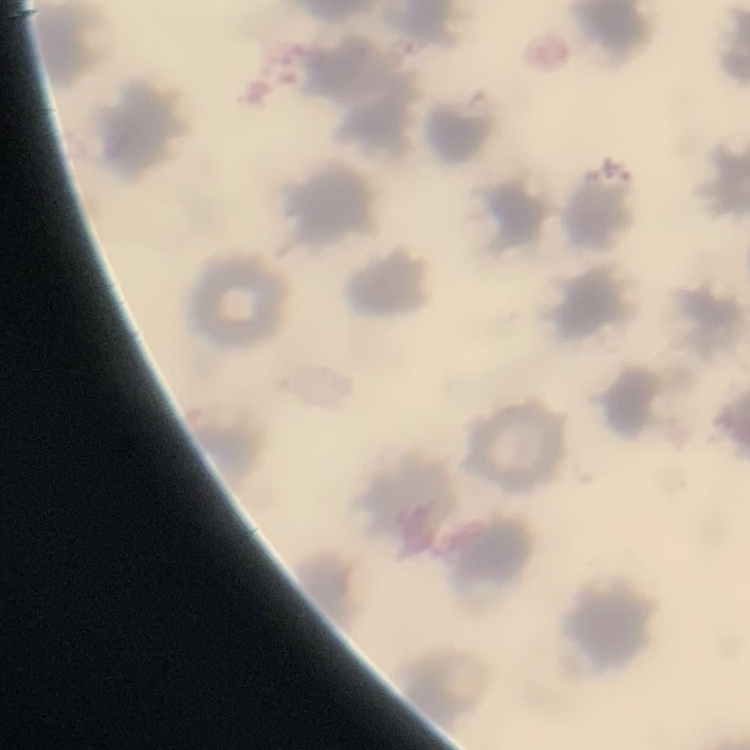
red_blood_cell_morphology: no rouleaux formation
stain: Field's or Giemsa
preparation: thin peripheral smear
image_type: one tile cut from a larger photomicrograph